Classify this cell by malaria status.
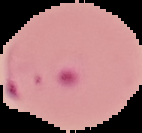
It is parasitized.

From a thin blood smear. Cell region segmented out of the field of view; the surrounding area is masked to black. Image is 142×133 pixels.